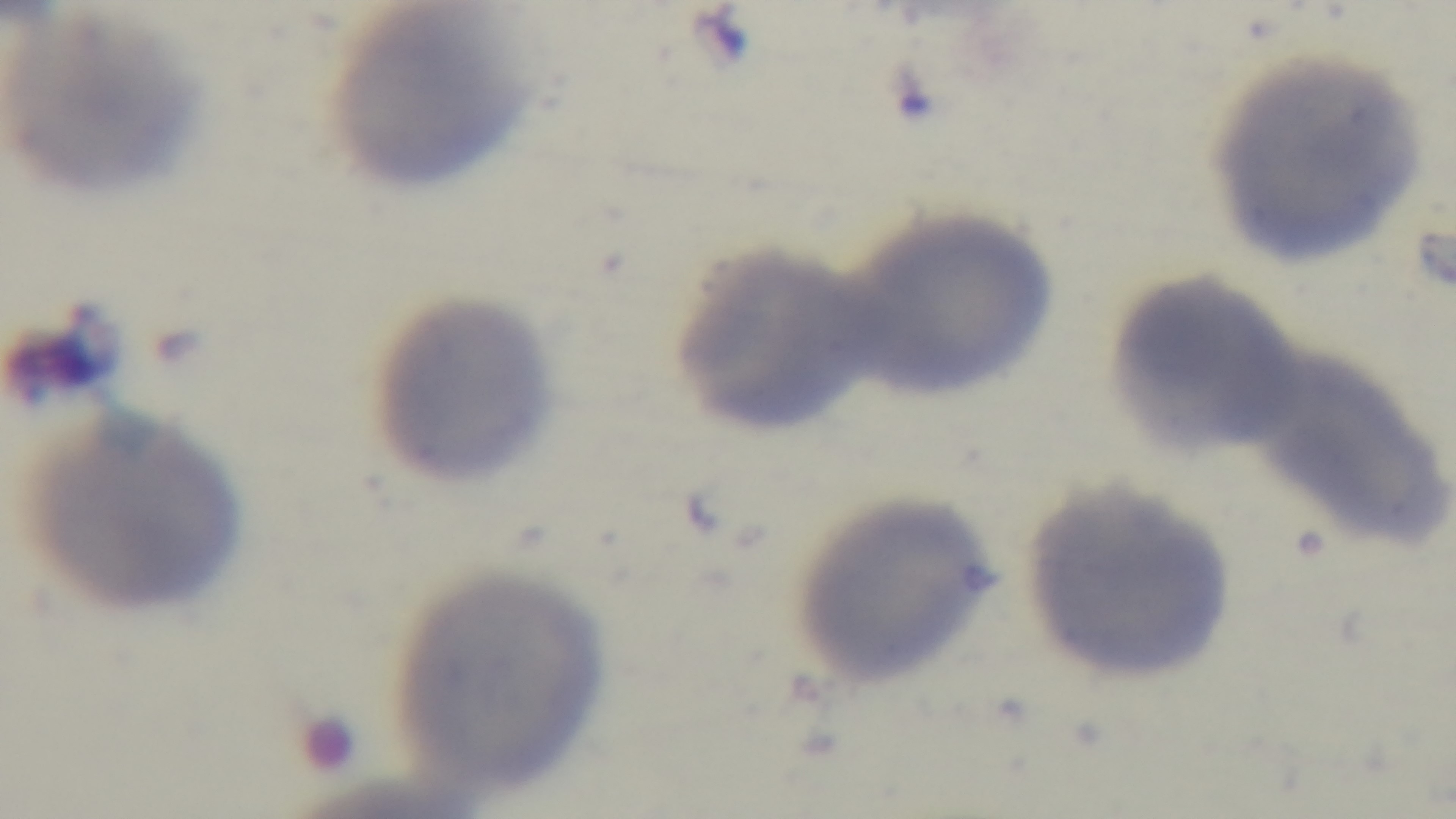
Oil-immersion objective, 100x. Mounted 4K digital camera. Single field of view. Malaria status: uninfected. Preparation: thin. Giemsa-stained. Light microscopy.